Assess this cell for malaria.
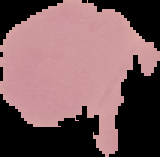

It is uninfected.

image type = segmented cell region on a black background
preparation = thin blood film
image size = 160×157 pixels